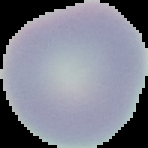 Cell region segmented out of the field of view; the surrounding area is masked to black. Image is 148×148 pixels. Result: negative for Plasmodium parasites. From a thin blood film.